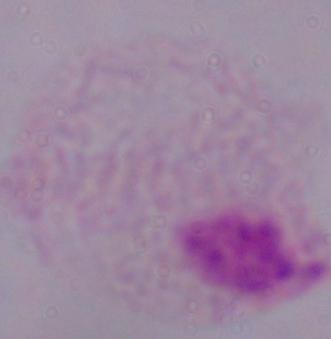
Micrograph. 1000x magnification. A trichomonad is seen.